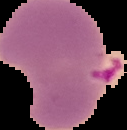

Summary:
  - Preparation: thin blood film
  - Image type: cell region segmented out of the field of view; surrounding area masked to black
  - Malaria status: parasitized
  - Image size: 127×130 pixels